Give the position of every Plasmodium parasite visible.
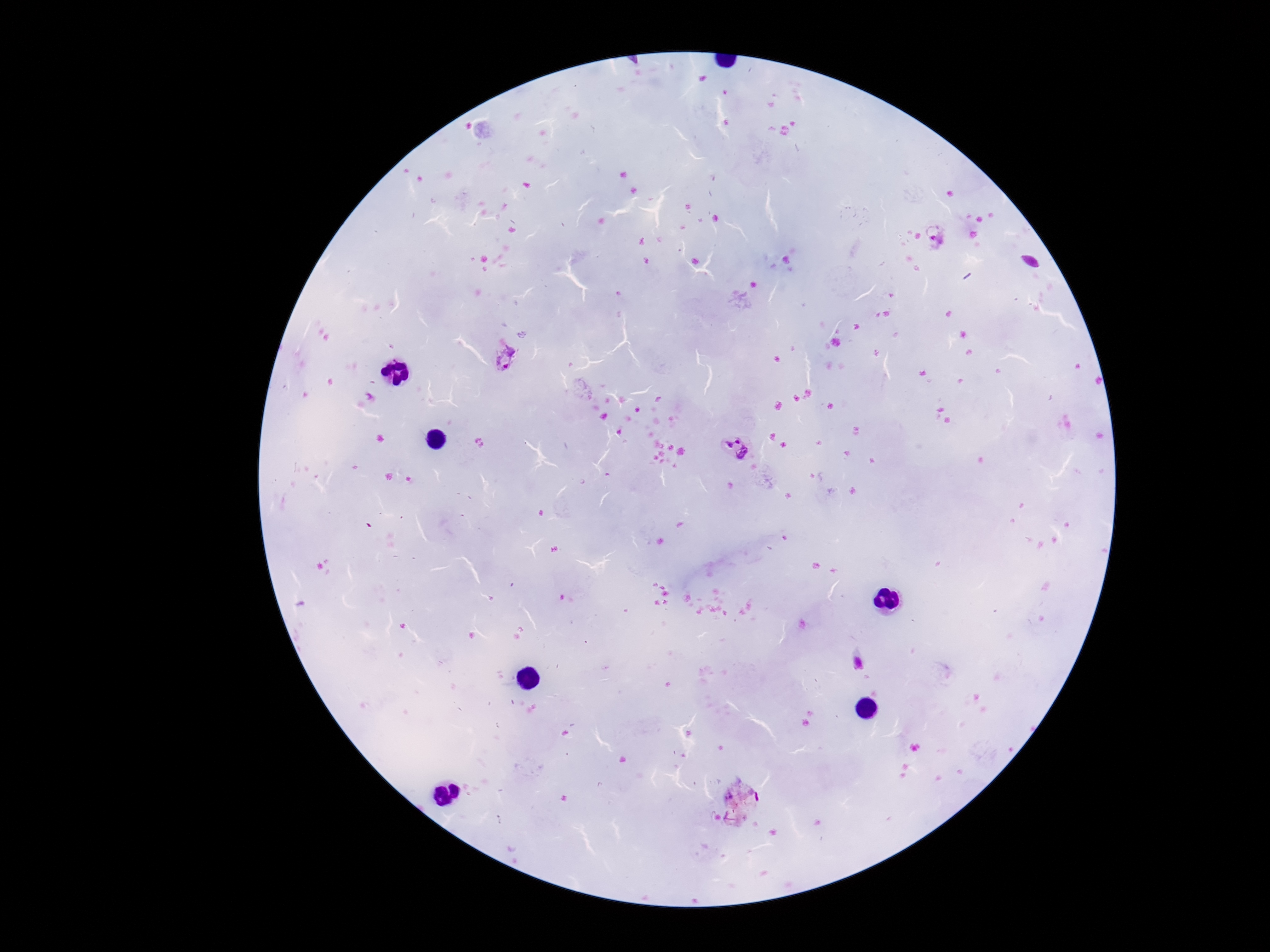

Approximate centers as (x, y) in pixels.
Plasmodium parasites: (935, 236), (507, 360), (744, 451).

Summary:
  - Stain: Giemsa
  - Preparation: thick blood smear
  - Image size: 1270×952 pixels
  - Capture: smartphone camera through the microscope eyepiece
  - Patient malaria status: infected
  - Magnification: 100x
  - Field of view: one from this slide